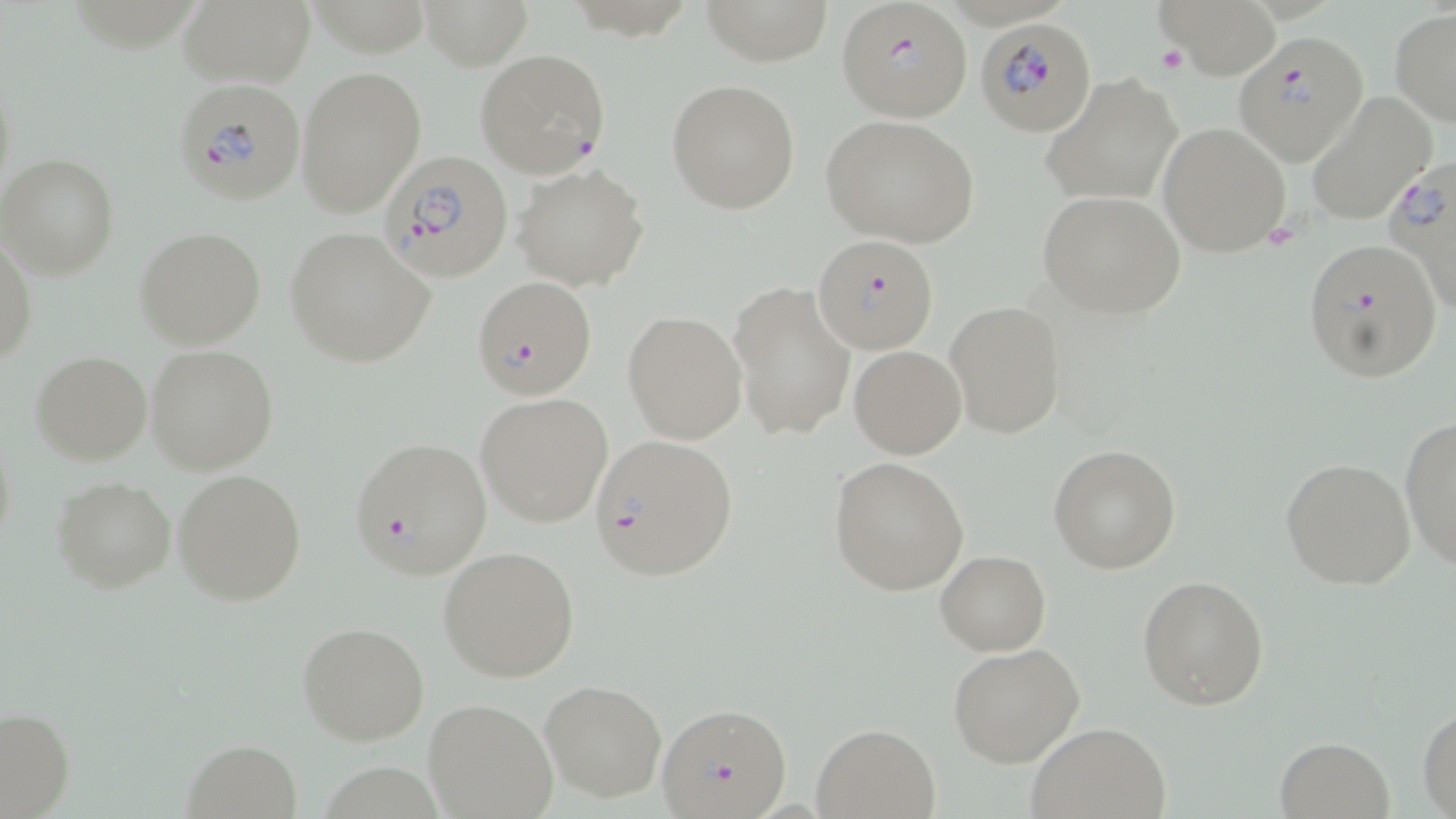
{
  "slide_level_diagnosis": "Plasmodium falciparum",
  "field_of_view": "one of a larger specimen",
  "modality": "light microscopy",
  "platelet_locations": "approximate bounding boxes as named x1/y1/x2/y2 corners in pixels: (x1=1156, y1=42, x2=1190, y2=76)",
  "stain": "May-Grünwald-Giemsa",
  "plasmodium_falciparum_infected_red_blood_cell_locations": "approximate bounding boxes as named x1/y1/x2/y2 corners in pixels: (x1=836, y1=3, x2=972, y2=124), (x1=976, y1=15, x2=1099, y2=135), (x1=1233, y1=31, x2=1368, y2=167), (x1=475, y1=48, x2=610, y2=179), (x1=174, y1=80, x2=306, y2=205), (x1=382, y1=153, x2=514, y2=281), (x1=1382, y1=161, x2=1456, y2=318), (x1=815, y1=236, x2=940, y2=354), (x1=1300, y1=236, x2=1442, y2=381), (x1=470, y1=277, x2=595, y2=400), (x1=589, y1=433, x2=739, y2=583), (x1=349, y1=435, x2=491, y2=579), (x1=659, y1=702, x2=791, y2=818)",
  "preparation": "thin blood smear",
  "magnification": "1000x",
  "image_size": "1456×819 pixels",
  "uninfected_red_blood_cell_locations": "approximate bounding boxes as named x1/y1/x2/y2 corners in pixels: (x1=176, y1=0, x2=315, y2=89), (x1=418, y1=0, x2=533, y2=69), (x1=1156, y1=0, x2=1287, y2=78), (x1=1389, y1=8, x2=1456, y2=126), (x1=295, y1=64, x2=427, y2=218), (x1=1041, y1=74, x2=1184, y2=205), (x1=666, y1=78, x2=801, y2=215), (x1=1304, y1=93, x2=1434, y2=226), (x1=821, y1=113, x2=982, y2=249), (x1=1159, y1=122, x2=1292, y2=258), (x1=0, y1=153, x2=120, y2=279), (x1=513, y1=164, x2=650, y2=290), (x1=1036, y1=189, x2=1186, y2=318), (x1=136, y1=227, x2=266, y2=350), (x1=285, y1=228, x2=434, y2=366), (x1=0, y1=233, x2=36, y2=371), (x1=728, y1=282, x2=855, y2=442), (x1=946, y1=301, x2=1066, y2=439), (x1=622, y1=312, x2=747, y2=444), (x1=146, y1=344, x2=278, y2=475), (x1=849, y1=345, x2=966, y2=459), (x1=29, y1=351, x2=152, y2=465), (x1=476, y1=393, x2=613, y2=527), (x1=1400, y1=415, x2=1456, y2=567), (x1=1, y1=424, x2=18, y2=564), (x1=1049, y1=444, x2=1180, y2=574), (x1=828, y1=455, x2=970, y2=596), (x1=1280, y1=456, x2=1416, y2=591), (x1=173, y1=469, x2=307, y2=606), (x1=51, y1=475, x2=177, y2=595), (x1=438, y1=546, x2=580, y2=682), (x1=936, y1=548, x2=1051, y2=655), (x1=1137, y1=573, x2=1269, y2=710), (x1=296, y1=622, x2=430, y2=746), (x1=948, y1=643, x2=1085, y2=769), (x1=541, y1=680, x2=665, y2=802), (x1=425, y1=699, x2=558, y2=818), (x1=1417, y1=704, x2=1456, y2=815), (x1=0, y1=705, x2=74, y2=817), (x1=1026, y1=721, x2=1172, y2=818), (x1=812, y1=723, x2=941, y2=818), (x1=1274, y1=736, x2=1394, y2=818), (x1=182, y1=737, x2=304, y2=817)"
}